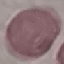

Malaria status: uninfected. Cell patch, automatically extracted from a larger field of view and resized to 64 × 64 pixels. Thin blood film. Acquired by smartphone through the microscope eyepiece. Giemsa stain.